Assess this cell for malaria.
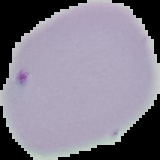

Uninfected.

image type = segmented cell region on a black background
image size = 160×160 pixels
preparation = thin blood smear